Point out Plasmodium parasites and leukocytes.
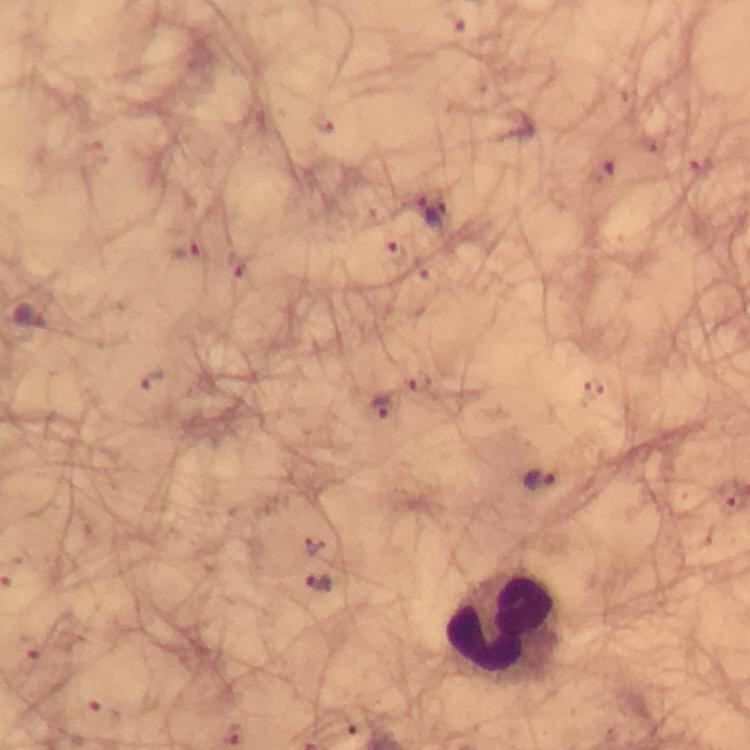

Approximate centers as [x, y] in pixels.
Plasmodium parasites: [453, 21], [187, 251], [396, 253], [31, 317], [153, 382], [381, 406], [540, 481], [730, 496], [312, 544], [320, 583], [30, 646], [102, 713].
Leukocytes: [499, 626].

Immersion oil applied. From a diagnostic examination for malaria. Photographed with a smartphone mounted on the microscope. Image is 750×750 pixels. 100x magnification. Giemsa stain. Cropped region of a single field of view. Thick blood smear.